Locate every Plasmodium parasite.
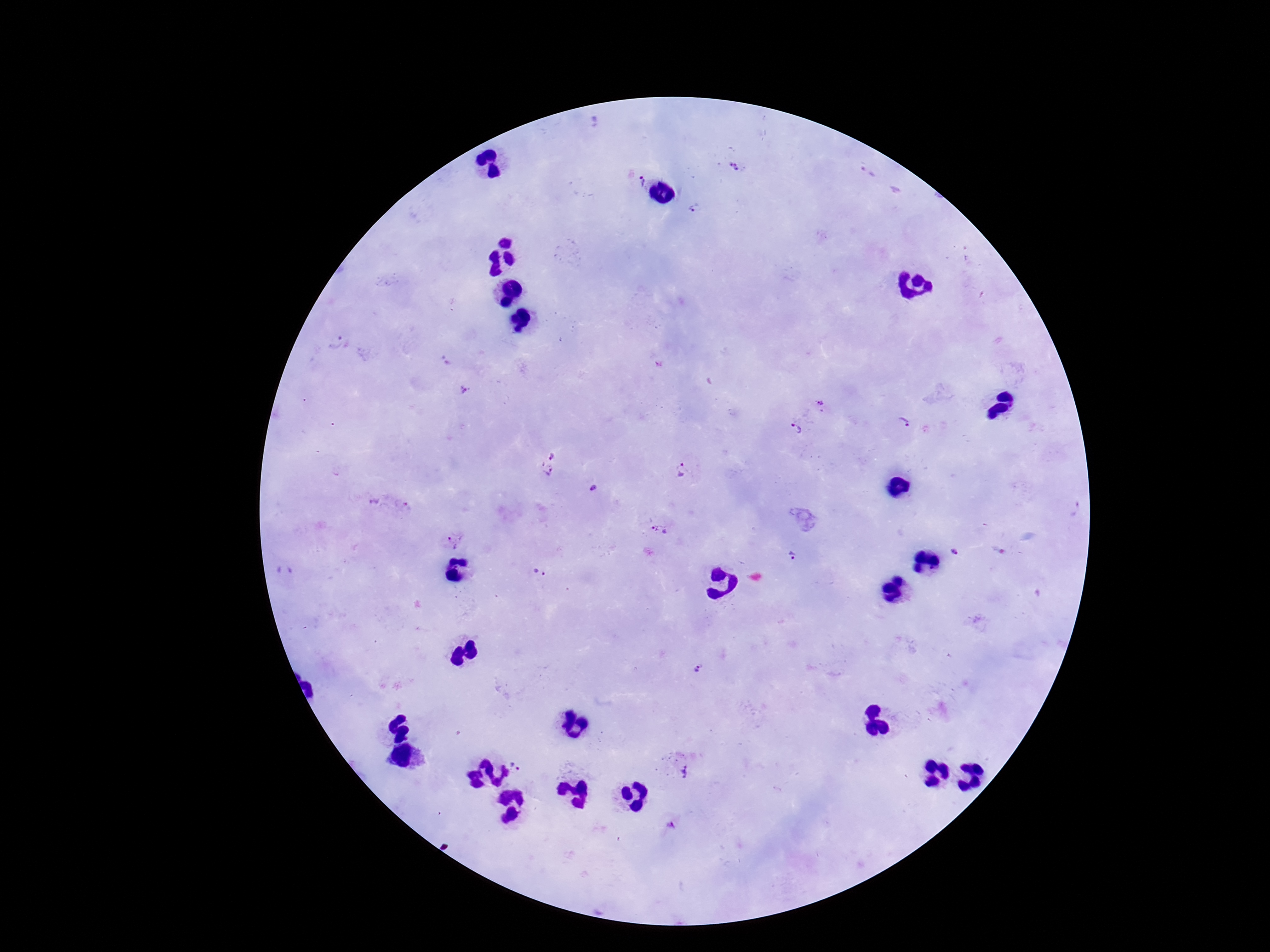
Approximate centers as {x, y} in pixels.
Plasmodium parasites: {734, 165}, {642, 179}, {695, 209}, {334, 342}, {464, 389}, {820, 405}, {905, 424}, {792, 431}, {550, 451}, {546, 470}, {680, 472}, {594, 490}, {372, 501}, {659, 531}, {454, 541}, {954, 551}, {793, 556}, {538, 573}, {697, 669}, {518, 761}, {683, 770}, {669, 825}.

Photographed through the microscope eyepiece with a smartphone camera. Thick peripheral-blood smear. Patient malaria status: infected. 100x magnification. Image is 1270×952 pixels. One field from this slide. Giemsa-stained preparation.